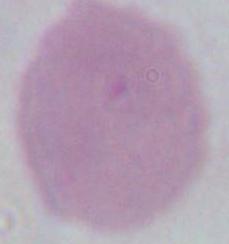
{
  "magnification": "1000x",
  "modality": "micrograph",
  "identification": "erythrocyte"
}